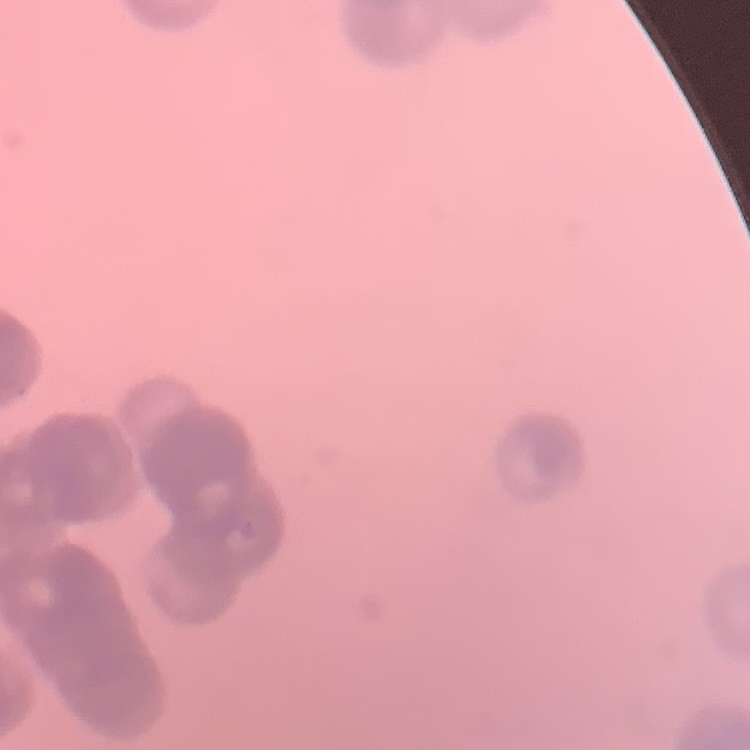 The red blood cells exhibit rouleaux formation. Thin peripheral smear. One tile cut from a larger photomicrograph. Stained with either Field's or Giemsa.